Locate and identify every blood parasite.
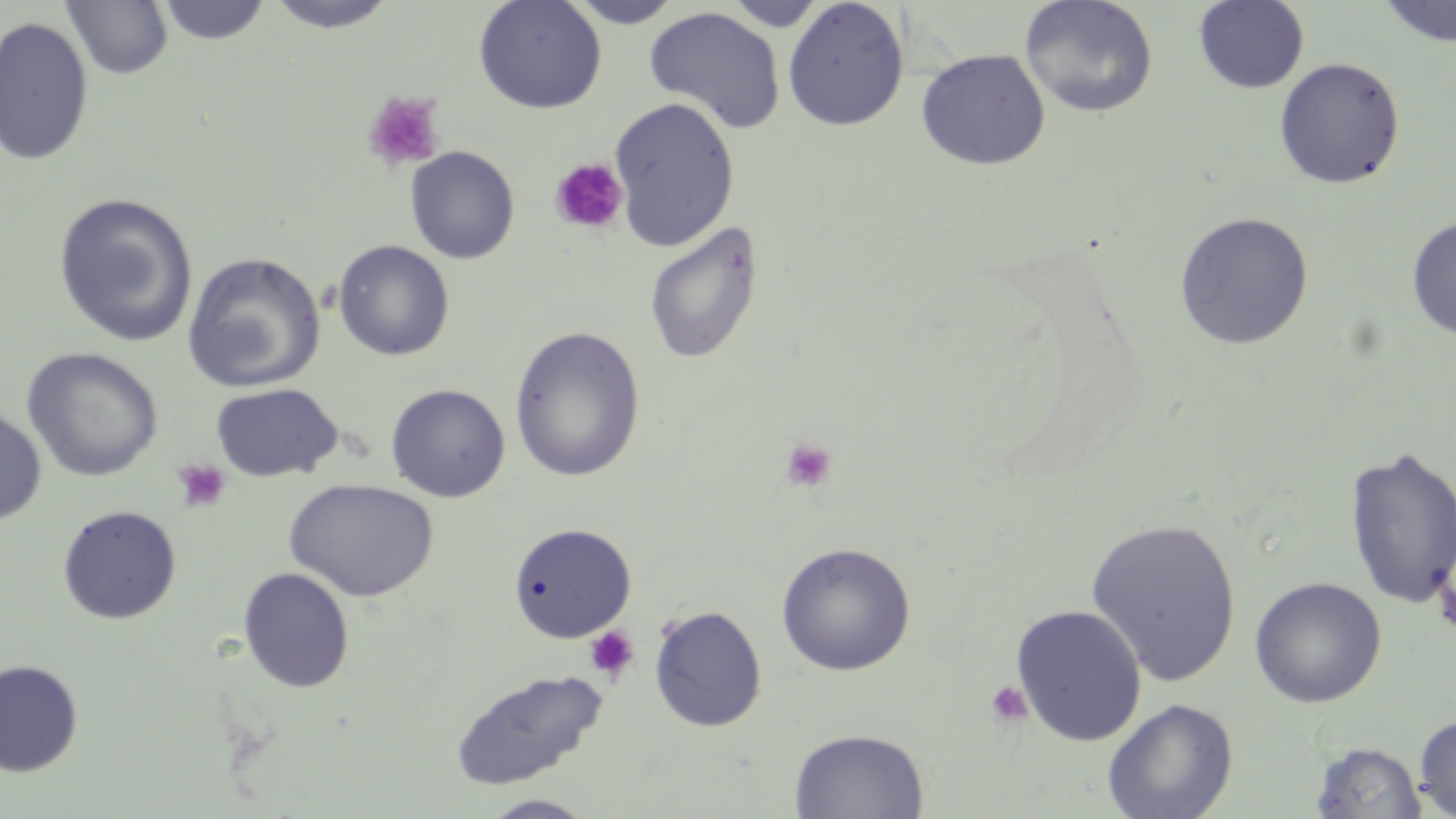

No blood parasites seen.

Approximate bounding boxes as (x1, y1, x2, y2) in pixels. Platelet locations: (363, 90, 446, 173), (549, 158, 628, 235), (779, 437, 837, 493), (171, 457, 232, 514), (583, 625, 639, 684), (983, 679, 1034, 730). Uninfected red blood cell locations: (263, 0, 400, 33), (473, 0, 607, 115), (724, 0, 826, 31), (782, 0, 910, 131), (1020, 0, 1159, 118), (1193, 0, 1309, 93), (61, 1, 173, 80), (156, 1, 273, 46), (564, 1, 683, 28), (1377, 1, 1456, 47), (644, 7, 786, 134), (0, 15, 94, 167), (915, 47, 1051, 170), (1273, 57, 1407, 190), (608, 96, 740, 253), (404, 145, 520, 264), (52, 192, 199, 348), (1173, 211, 1314, 349), (1406, 216, 1456, 341), (643, 220, 763, 366), (332, 240, 455, 361), (182, 252, 326, 393), (509, 326, 645, 482), (21, 347, 164, 482), (210, 382, 343, 482), (386, 383, 510, 502), (0, 404, 47, 527), (1344, 443, 1456, 610), (283, 478, 438, 601), (57, 505, 182, 625), (1085, 517, 1243, 686), (508, 522, 637, 642), (775, 542, 916, 676), (238, 567, 355, 693), (1249, 576, 1387, 708), (1010, 603, 1147, 746), (648, 604, 767, 732), (0, 658, 84, 778), (449, 667, 608, 790), (1101, 697, 1239, 819), (1414, 713, 1456, 817), (789, 728, 929, 818), (1309, 741, 1428, 819), (480, 794, 599, 819). Slide-level diagnosis: negative for blood parasites. Light microscopy. May-Grünwald-Giemsa-stained preparation. Image is 1456×819 pixels. 1000x magnification. One field of a larger specimen. Thin blood film.